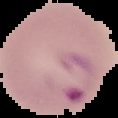
preparation = thin blood film
image type = segmented cell region on a black background
image size = 118×118 pixels
malaria status = parasitized